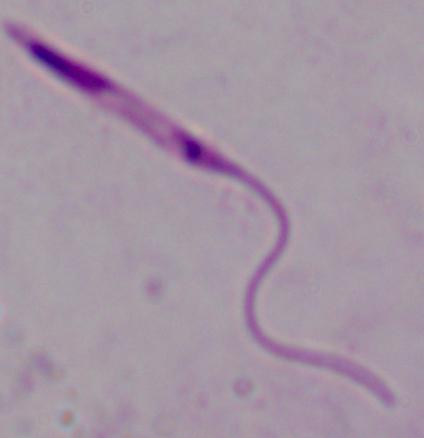

magnification = 1000x
modality = photomicrograph
identification = Leishmania